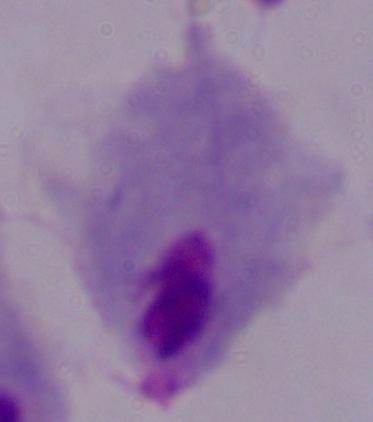
Summary:
  - Modality: micrograph
  - Magnification: 1000x
  - Identification: trichomonad